Locate every blood parasite and identify its species.
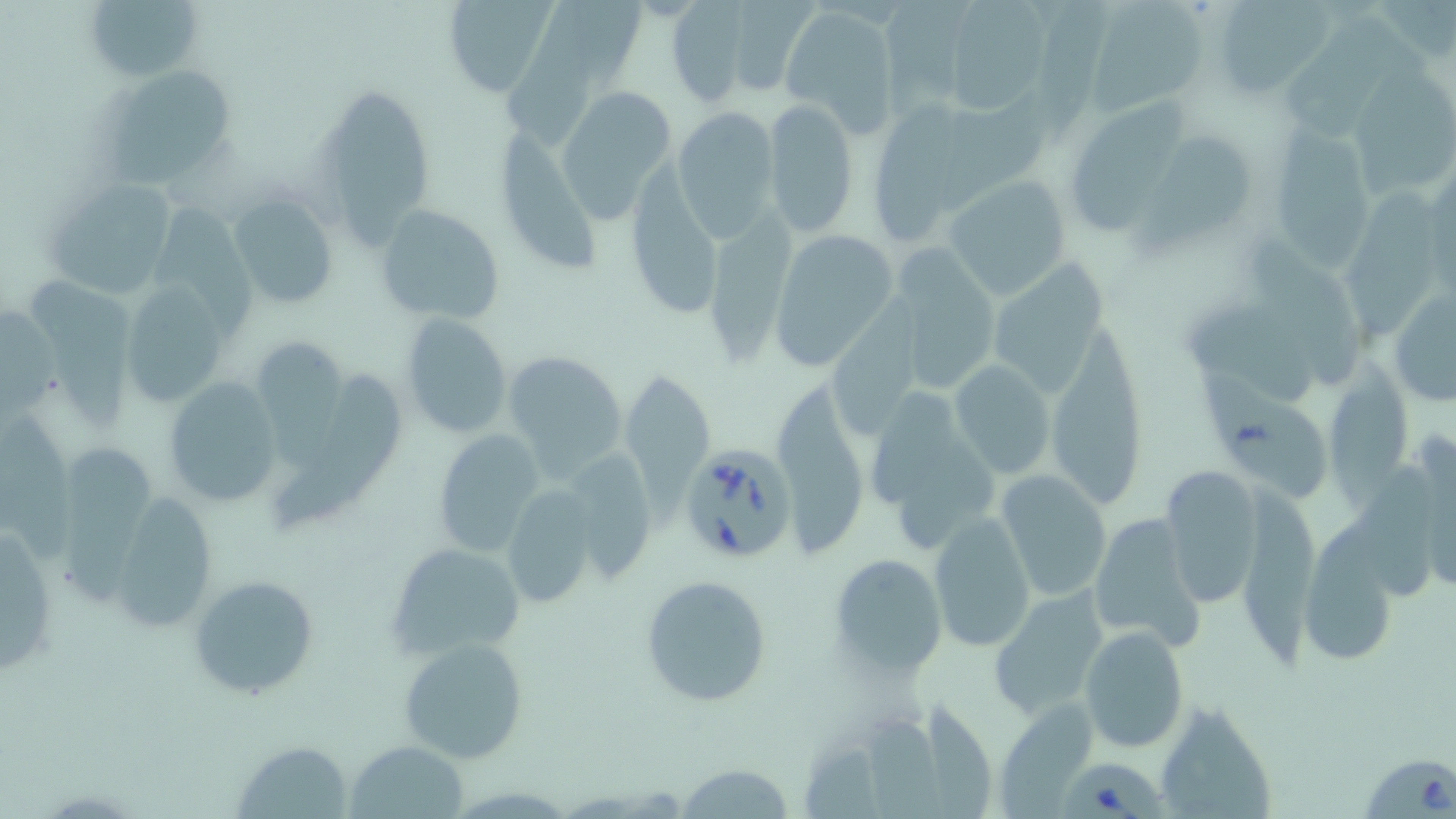

Approximate bounding boxes as named x1/y1/x2/y2 corners in pixels.
Babesia divergens-infected red blood cells: (x1=678, y1=440, x2=799, y2=564), (x1=1362, y1=751, x2=1455, y2=818), (x1=1057, y1=758, x2=1162, y2=819).
No Plasmodium falciparum, Plasmodium ovale, Plasmodium malariae, Plasmodium vivax, or Trypanosoma brucei observed.

Summary:
  - Uninfected red blood cell locations: (x1=90, y1=0, x2=202, y2=77), (x1=441, y1=0, x2=559, y2=96), (x1=502, y1=0, x2=602, y2=147), (x1=532, y1=0, x2=649, y2=84), (x1=731, y1=0, x2=821, y2=95), (x1=880, y1=0, x2=980, y2=113), (x1=1038, y1=0, x2=1116, y2=146), (x1=1209, y1=0, x2=1331, y2=98), (x1=1085, y1=1, x2=1211, y2=117), (x1=661, y1=2, x2=755, y2=106), (x1=944, y1=3, x2=1053, y2=116), (x1=781, y1=5, x2=898, y2=133), (x1=1285, y1=11, x2=1407, y2=138), (x1=104, y1=64, x2=243, y2=189), (x1=1352, y1=64, x2=1456, y2=201), (x1=555, y1=85, x2=679, y2=222), (x1=327, y1=90, x2=433, y2=256), (x1=939, y1=97, x2=1049, y2=220), (x1=764, y1=99, x2=859, y2=237), (x1=1076, y1=99, x2=1196, y2=223), (x1=867, y1=101, x2=986, y2=238), (x1=670, y1=105, x2=781, y2=240), (x1=1277, y1=122, x2=1375, y2=277), (x1=495, y1=129, x2=608, y2=274), (x1=1139, y1=138, x2=1253, y2=251), (x1=632, y1=162, x2=716, y2=320), (x1=941, y1=175, x2=1073, y2=302), (x1=44, y1=176, x2=179, y2=297), (x1=1345, y1=181, x2=1439, y2=346), (x1=227, y1=193, x2=338, y2=310), (x1=707, y1=201, x2=800, y2=365), (x1=374, y1=203, x2=505, y2=324), (x1=148, y1=207, x2=258, y2=340), (x1=1243, y1=227, x2=1359, y2=385), (x1=767, y1=230, x2=900, y2=372), (x1=883, y1=249, x2=999, y2=395), (x1=990, y1=253, x2=1117, y2=398), (x1=26, y1=274, x2=143, y2=431), (x1=1389, y1=282, x2=1456, y2=409), (x1=119, y1=283, x2=226, y2=408), (x1=1178, y1=295, x2=1327, y2=408), (x1=827, y1=299, x2=923, y2=447), (x1=0, y1=308, x2=63, y2=423), (x1=401, y1=311, x2=513, y2=440), (x1=1047, y1=323, x2=1149, y2=513), (x1=250, y1=341, x2=344, y2=464), (x1=502, y1=349, x2=627, y2=481), (x1=1321, y1=349, x2=1409, y2=507), (x1=952, y1=360, x2=1056, y2=479), (x1=1183, y1=361, x2=1333, y2=506), (x1=620, y1=367, x2=712, y2=504), (x1=273, y1=369, x2=406, y2=531), (x1=161, y1=379, x2=283, y2=510), (x1=776, y1=380, x2=874, y2=556), (x1=873, y1=391, x2=955, y2=512), (x1=0, y1=407, x2=76, y2=562), (x1=431, y1=429, x2=546, y2=558), (x1=896, y1=437, x2=998, y2=558), (x1=56, y1=441, x2=153, y2=604), (x1=569, y1=447, x2=654, y2=587), (x1=1358, y1=458, x2=1437, y2=600), (x1=1158, y1=464, x2=1264, y2=609), (x1=994, y1=470, x2=1112, y2=602), (x1=1245, y1=480, x2=1321, y2=674), (x1=498, y1=487, x2=603, y2=611), (x1=105, y1=488, x2=219, y2=633), (x1=1086, y1=509, x2=1207, y2=653), (x1=927, y1=511, x2=1037, y2=651), (x1=1, y1=521, x2=57, y2=683), (x1=385, y1=541, x2=527, y2=663), (x1=1299, y1=549, x2=1397, y2=663), (x1=825, y1=555, x2=948, y2=677), (x1=189, y1=573, x2=318, y2=699), (x1=639, y1=573, x2=773, y2=709), (x1=985, y1=589, x2=1107, y2=720), (x1=1079, y1=626, x2=1190, y2=754), (x1=398, y1=636, x2=529, y2=764), (x1=925, y1=699, x2=994, y2=819), (x1=1153, y1=700, x2=1278, y2=819), (x1=996, y1=701, x2=1095, y2=819), (x1=862, y1=710, x2=949, y2=819), (x1=802, y1=737, x2=882, y2=819), (x1=230, y1=738, x2=354, y2=817), (x1=347, y1=739, x2=468, y2=818), (x1=675, y1=762, x2=796, y2=818)
  - Slide-level diagnosis: Babesia divergens
  - Magnification: 1000x
  - Modality: light microscopy
  - Preparation: thin blood smear
  - Image size: 1456×819 pixels
  - Stain: May-Grünwald-Giemsa
  - Field of view: one of a larger specimen